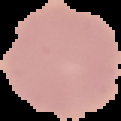
From a thin blood smear. Image is 121×121 pixels. Segmented cell region on a black background. Result: negative for malaria parasites.